State the blood parasite species.
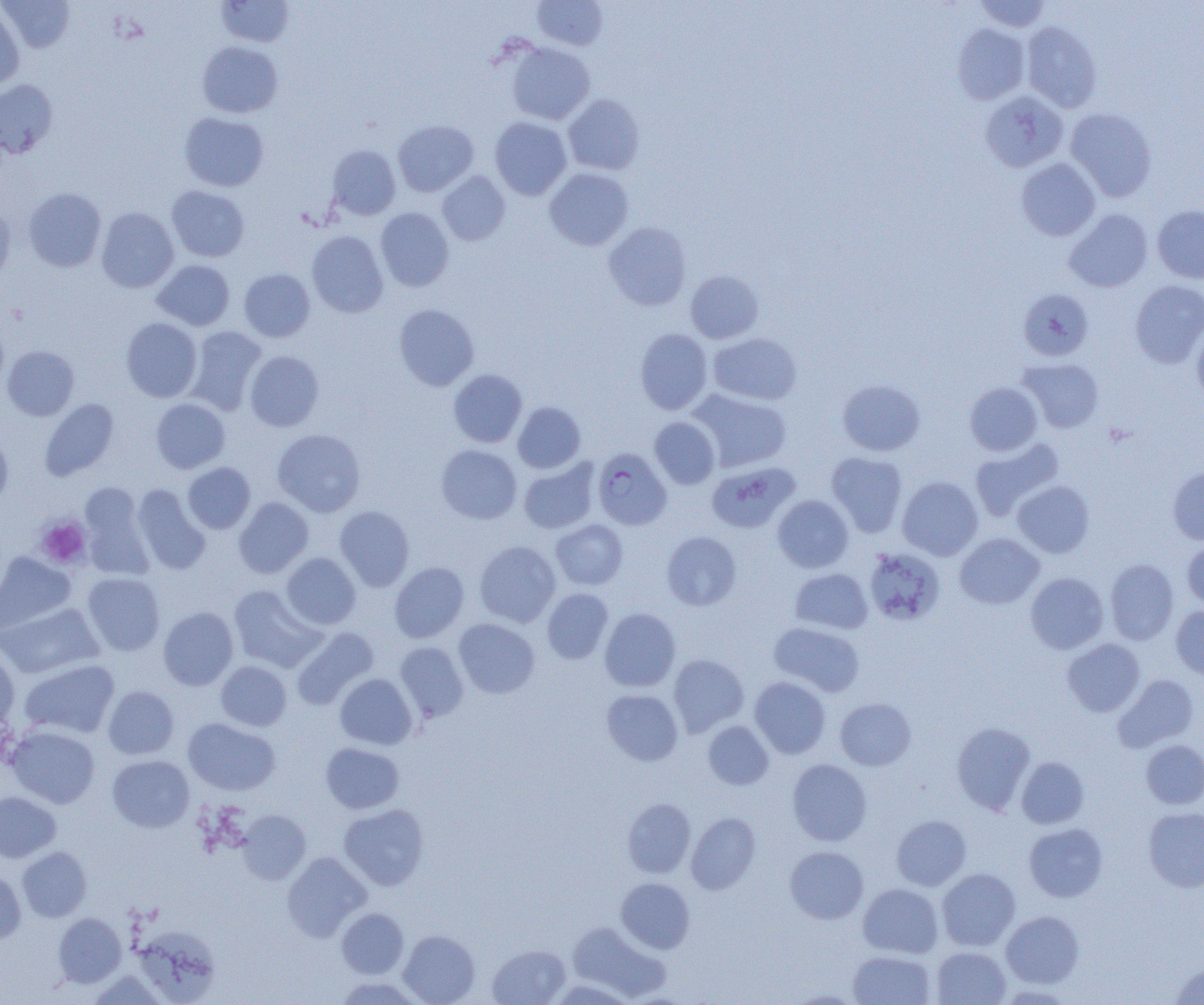

Plasmodium falciparum.

Summary:
  - Coordinate format: approximate bounding boxes as [x1, y1, x2, y2] in pixels
  - Uninfected red blood cell locations: [215, 0, 295, 47], [532, 0, 607, 50], [975, 0, 1051, 32], [1, 1, 75, 53], [0, 4, 25, 90], [1022, 21, 1102, 112], [953, 23, 1031, 105], [197, 41, 283, 118], [506, 43, 594, 125], [0, 79, 58, 158], [979, 90, 1068, 172], [562, 93, 645, 175], [1065, 107, 1157, 201], [179, 112, 269, 191], [489, 116, 572, 200], [393, 119, 478, 197], [327, 144, 401, 219], [1016, 158, 1101, 241], [544, 168, 633, 250], [437, 171, 510, 245], [167, 185, 249, 262], [23, 188, 107, 272], [0, 203, 16, 284], [1153, 205, 1204, 283], [96, 207, 179, 293], [376, 207, 454, 291], [1064, 209, 1153, 292], [603, 221, 692, 310], [306, 230, 388, 317], [152, 260, 235, 330], [239, 268, 315, 342], [685, 270, 764, 343], [1130, 280, 1204, 368], [1018, 288, 1094, 361], [394, 304, 479, 391], [0, 311, 9, 393], [121, 317, 202, 402], [1191, 321, 1204, 402], [185, 326, 266, 415], [635, 328, 712, 415], [709, 333, 802, 405], [2, 346, 79, 420], [244, 351, 324, 431], [1018, 358, 1104, 433], [448, 369, 527, 447], [837, 379, 925, 456], [964, 382, 1043, 456], [689, 389, 792, 472], [39, 398, 120, 481], [151, 399, 230, 473], [513, 401, 585, 473], [649, 417, 720, 488], [0, 428, 13, 507], [272, 428, 365, 517], [970, 438, 1064, 520], [436, 444, 522, 524], [826, 452, 908, 538], [518, 459, 599, 534], [182, 462, 255, 534], [707, 462, 798, 533], [1167, 465, 1204, 545], [897, 476, 983, 560], [1013, 481, 1095, 557], [80, 484, 151, 577], [132, 484, 210, 574], [773, 495, 853, 573], [233, 497, 313, 578], [334, 506, 415, 591], [551, 519, 628, 590], [661, 531, 741, 610], [955, 533, 1044, 609], [1182, 539, 1204, 610], [474, 540, 560, 627], [864, 547, 945, 625], [0, 551, 76, 633], [281, 552, 361, 629], [1105, 558, 1179, 645], [389, 562, 470, 642], [790, 568, 873, 634], [82, 572, 165, 655], [1025, 572, 1108, 654], [228, 585, 325, 671], [542, 589, 613, 664], [1, 602, 103, 678], [1171, 605, 1204, 678], [158, 606, 238, 690], [600, 608, 680, 692], [454, 618, 539, 698], [769, 622, 865, 697], [292, 627, 379, 709], [1062, 638, 1145, 716], [395, 642, 469, 722], [0, 647, 20, 728], [668, 654, 749, 736], [19, 659, 120, 739], [215, 661, 292, 731], [335, 673, 417, 749], [1114, 674, 1198, 752], [750, 676, 831, 759], [103, 686, 179, 759], [602, 689, 683, 766], [835, 698, 916, 770], [183, 718, 280, 795], [703, 721, 773, 790], [951, 722, 1035, 814], [5, 725, 100, 808], [1141, 739, 1204, 809], [320, 743, 404, 814], [107, 755, 194, 832], [1017, 757, 1089, 829], [787, 759, 872, 846], [0, 791, 61, 862], [622, 798, 696, 878], [338, 804, 429, 890], [1143, 808, 1204, 891], [237, 809, 311, 884], [686, 812, 761, 895], [891, 815, 971, 891], [1024, 823, 1108, 902], [17, 846, 92, 922], [785, 846, 869, 924], [282, 853, 371, 941], [937, 868, 1020, 950], [0, 870, 26, 943], [616, 877, 695, 953], [858, 883, 943, 958], [336, 907, 409, 978], [1001, 911, 1083, 987], [53, 913, 126, 987], [566, 922, 671, 1001], [132, 923, 222, 1004], [398, 930, 480, 1004], [487, 944, 570, 1005], [932, 947, 1011, 1005], [847, 951, 935, 1005], [1170, 962, 1204, 1005], [89, 971, 167, 1005], [333, 976, 423, 1005], [788, 990, 863, 1004]
  - Plasmodium falciparum-infected red blood cell locations: [592, 448, 672, 530]
  - Platelet locations: [36, 518, 91, 568]
  - Magnification: 1000x
  - Preparation: thin blood smear
  - Field of view: one of a larger specimen
  - Image size: 1204×1005 pixels
  - Modality: light microscopy